Report the malaria status of this cell.
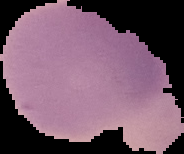

Uninfected.

image_size: 184×154 pixels
preparation: thin blood smear
image_type: cell region segmented out of the field of view; surrounding area masked to black